Give the extent of all Plasmodium ovale-infected red blood cells.
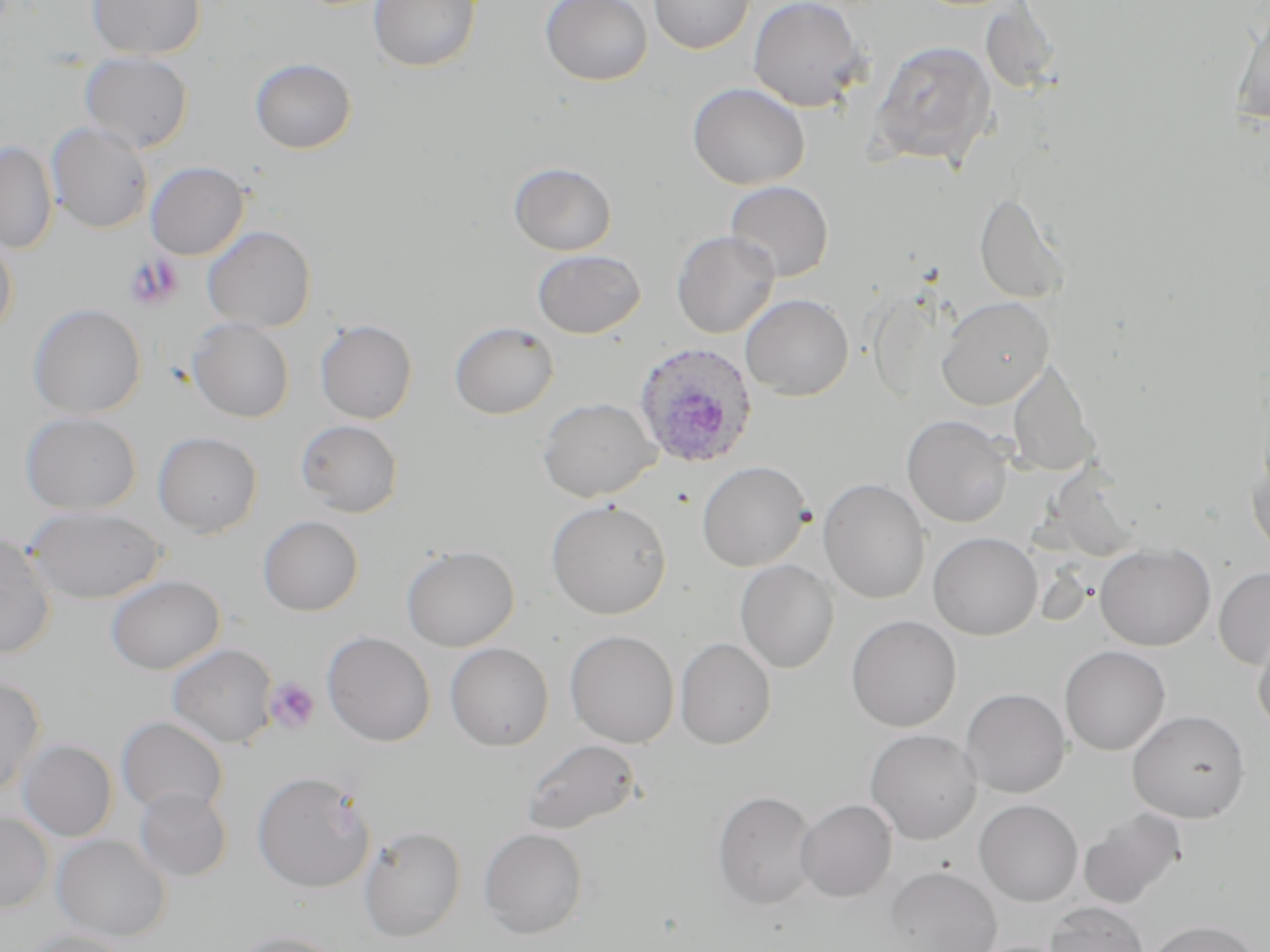

Approximate bounding boxes as (x1, y1, x2, y2) in pixels.
Plasmodium ovale-infected red blood cells: (632, 341, 758, 470).

slide-level diagnosis = Plasmodium ovale
platelet locations = approximate bounding boxes as (x1, y1, x2, y2) in pixels: (265, 677, 320, 734)
stain = May-Grünwald-Giemsa
field of view = single
preparation = thin blood film
uninfected red blood cell locations = approximate bounding boxes as (x1, y1, x2, y2) in pixels: (87, 0, 206, 59), (368, 0, 481, 72), (540, 0, 653, 86), (649, 0, 755, 54), (747, 0, 868, 112), (979, 2, 1063, 96), (1230, 8, 1270, 124), (868, 40, 997, 168), (79, 54, 193, 153), (250, 57, 357, 154), (687, 83, 810, 190), (46, 123, 153, 233), (0, 140, 57, 254), (146, 161, 249, 260), (508, 162, 617, 256), (726, 180, 833, 281), (974, 191, 1071, 305), (202, 226, 315, 332), (672, 230, 780, 338), (0, 233, 18, 338), (532, 249, 645, 338), (740, 294, 853, 400), (936, 297, 1054, 409), (28, 303, 146, 419), (186, 318, 294, 422), (315, 319, 418, 424), (450, 321, 559, 419), (1006, 361, 1100, 478), (537, 397, 660, 502), (20, 411, 141, 514), (902, 415, 1013, 527), (296, 419, 404, 517), (153, 431, 262, 537), (1247, 444, 1270, 557), (697, 461, 811, 572), (819, 478, 930, 605), (546, 499, 671, 619), (25, 505, 165, 603), (258, 515, 363, 616), (0, 532, 56, 659), (928, 532, 1042, 640), (1095, 543, 1215, 651), (401, 544, 520, 651), (735, 559, 839, 673), (1214, 566, 1270, 669), (106, 574, 225, 674), (845, 615, 962, 732), (1252, 626, 1270, 734), (565, 630, 679, 747), (322, 631, 436, 746), (675, 638, 776, 749), (445, 642, 554, 751), (167, 643, 278, 748), (1059, 645, 1170, 755), (0, 676, 46, 795), (960, 687, 1070, 798), (1127, 709, 1251, 822), (116, 716, 228, 816), (866, 728, 981, 844), (521, 738, 643, 836), (18, 739, 118, 841), (251, 770, 375, 893), (134, 787, 232, 881), (713, 790, 818, 910), (795, 799, 897, 902), (974, 799, 1083, 906), (1078, 807, 1186, 909), (0, 811, 54, 913), (359, 826, 466, 942), (479, 827, 588, 939), (52, 834, 171, 942), (886, 866, 1001, 952), (1045, 901, 1149, 952), (1146, 920, 1262, 952), (19, 928, 132, 952), (230, 930, 345, 952)
magnification = 1000x
modality = optical microscopy
image size = 1270×952 pixels